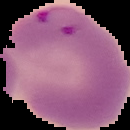

{
  "image_type": "segmented cell region on a black background",
  "preparation": "thin blood smear",
  "result": "malaria parasites detected",
  "image_size": "130×130 pixels"
}